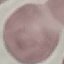

Summary:
  - Malaria status: uninfected
  - Image type: cell patch, automatically extracted from a larger field of view and resized to 64 × 64 pixels
  - Capture: smartphone camera at the microscope eyepiece
  - Stain: Giemsa
  - Preparation: thin blood smear